Report the malaria status of this cell.
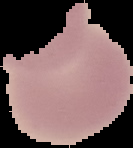

It is uninfected.

image size = 133×148 pixels
preparation = thin blood smear
image type = cell region segmented out of the field of view; surrounding area masked to black